Give the extent of all Plasmodium vivax-infected red blood cells.
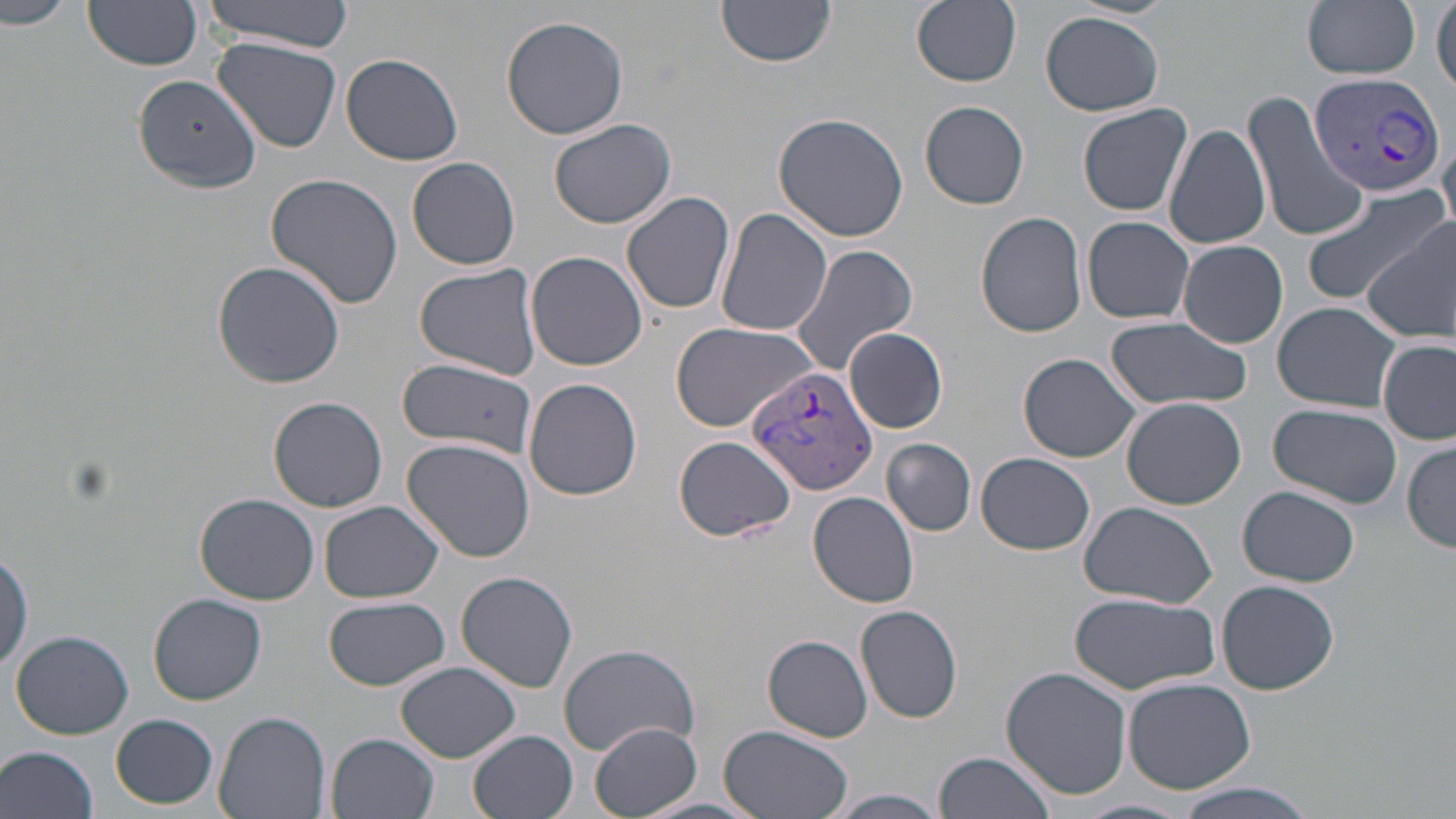
Approximate bounding boxes as named x1/y1/x2/y2 corners in pixels.
Plasmodium vivax-infected red blood cells: (x1=1309, y1=71, x2=1444, y2=200), (x1=746, y1=367, x2=881, y2=501).

Uninfected red blood cell locations: (x1=0, y1=0, x2=74, y2=32), (x1=202, y1=0, x2=356, y2=49), (x1=717, y1=0, x2=838, y2=69), (x1=912, y1=0, x2=1022, y2=88), (x1=1302, y1=0, x2=1422, y2=79), (x1=82, y1=1, x2=203, y2=72), (x1=1432, y1=4, x2=1455, y2=97), (x1=1040, y1=11, x2=1164, y2=117), (x1=501, y1=14, x2=629, y2=139), (x1=213, y1=37, x2=341, y2=151), (x1=341, y1=53, x2=463, y2=166), (x1=134, y1=73, x2=261, y2=194), (x1=1243, y1=90, x2=1369, y2=244), (x1=920, y1=100, x2=1030, y2=209), (x1=1077, y1=104, x2=1194, y2=217), (x1=773, y1=113, x2=910, y2=243), (x1=548, y1=118, x2=677, y2=231), (x1=1163, y1=123, x2=1271, y2=250), (x1=1439, y1=129, x2=1456, y2=234), (x1=409, y1=157, x2=521, y2=272), (x1=265, y1=172, x2=405, y2=310), (x1=1302, y1=185, x2=1447, y2=309), (x1=622, y1=191, x2=736, y2=315), (x1=716, y1=209, x2=832, y2=338), (x1=974, y1=211, x2=1087, y2=337), (x1=1081, y1=217, x2=1196, y2=325), (x1=1365, y1=218, x2=1456, y2=343), (x1=1177, y1=241, x2=1287, y2=348), (x1=791, y1=245, x2=919, y2=377), (x1=526, y1=252, x2=648, y2=371), (x1=213, y1=261, x2=346, y2=388), (x1=413, y1=263, x2=544, y2=383), (x1=1273, y1=303, x2=1405, y2=413), (x1=1105, y1=317, x2=1250, y2=411), (x1=670, y1=322, x2=816, y2=431), (x1=846, y1=327, x2=948, y2=434), (x1=1379, y1=338, x2=1455, y2=446), (x1=1018, y1=353, x2=1141, y2=462), (x1=398, y1=362, x2=534, y2=455), (x1=524, y1=379, x2=643, y2=501), (x1=268, y1=396, x2=388, y2=514), (x1=1121, y1=396, x2=1247, y2=509), (x1=1268, y1=403, x2=1402, y2=509), (x1=673, y1=435, x2=797, y2=543), (x1=402, y1=439, x2=536, y2=563), (x1=883, y1=439, x2=975, y2=535), (x1=1404, y1=441, x2=1456, y2=552), (x1=977, y1=452, x2=1095, y2=556), (x1=1239, y1=486, x2=1363, y2=588), (x1=808, y1=491, x2=919, y2=608), (x1=194, y1=495, x2=319, y2=605), (x1=319, y1=501, x2=444, y2=604), (x1=1079, y1=501, x2=1218, y2=608), (x1=0, y1=543, x2=33, y2=676), (x1=456, y1=572, x2=580, y2=693), (x1=1216, y1=579, x2=1340, y2=695), (x1=1069, y1=591, x2=1219, y2=695), (x1=151, y1=594, x2=268, y2=705), (x1=325, y1=598, x2=450, y2=691), (x1=855, y1=604, x2=965, y2=724), (x1=11, y1=630, x2=133, y2=740), (x1=763, y1=635, x2=873, y2=742), (x1=557, y1=644, x2=699, y2=757), (x1=397, y1=662, x2=520, y2=762), (x1=1001, y1=666, x2=1132, y2=798), (x1=1123, y1=677, x2=1256, y2=794), (x1=213, y1=709, x2=332, y2=819), (x1=111, y1=713, x2=218, y2=809), (x1=589, y1=720, x2=703, y2=818), (x1=720, y1=725, x2=853, y2=819), (x1=468, y1=730, x2=578, y2=818), (x1=328, y1=732, x2=438, y2=818), (x1=0, y1=744, x2=100, y2=819), (x1=934, y1=751, x2=1058, y2=819), (x1=1168, y1=779, x2=1321, y2=819), (x1=823, y1=789, x2=952, y2=819), (x1=1076, y1=798, x2=1197, y2=819). Slide-level diagnosis: Plasmodium vivax. 1000x magnification. Image is 1456×819 pixels. Single field of view. May-Grünwald-Giemsa-stained preparation. Thin blood film. Optical microscopy.